Outline platelets.
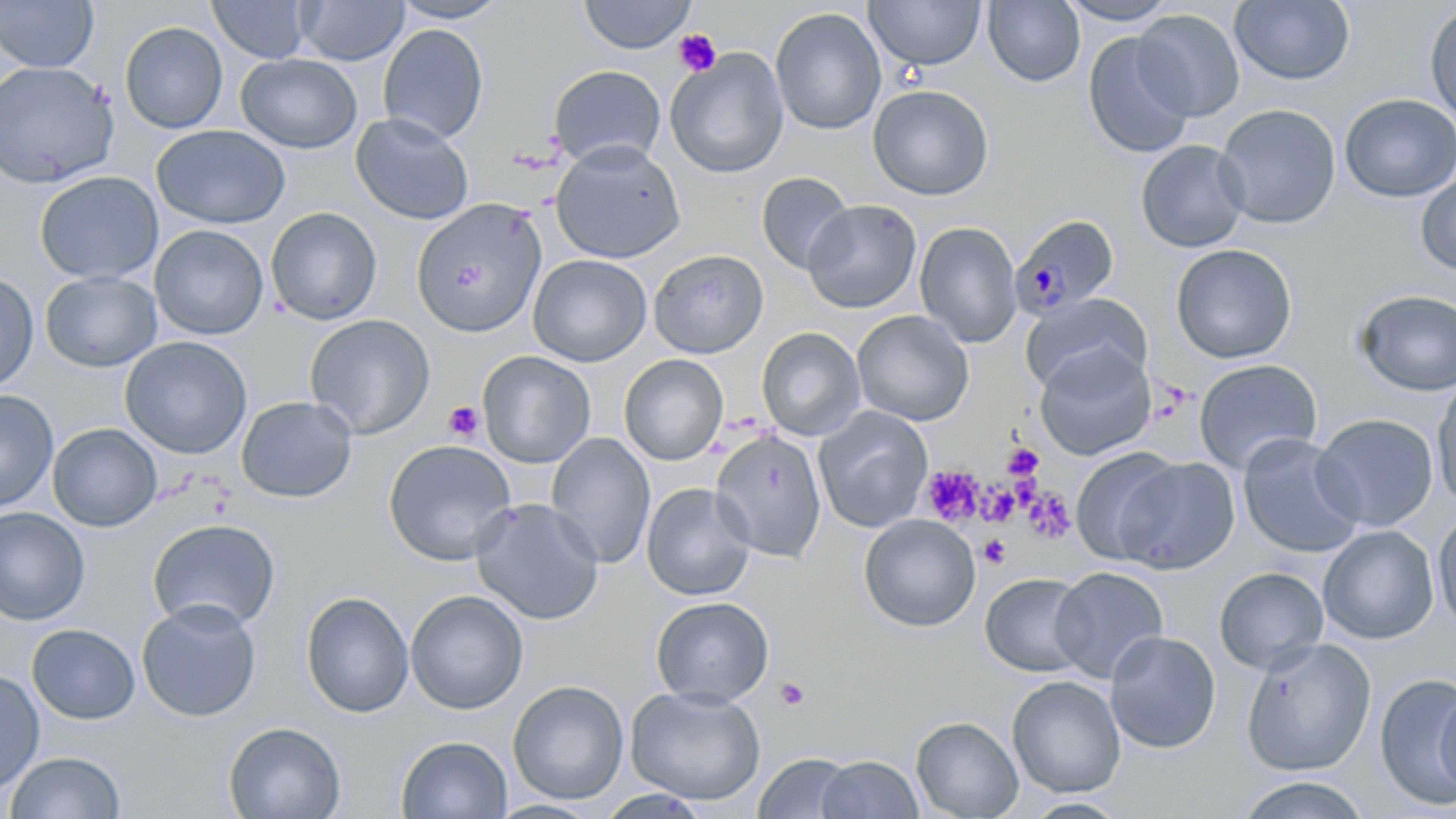
Approximate bounding boxes as (x1, y1, x2, y2) in pixels.
Platelets: (674, 29, 721, 76), (443, 401, 486, 443), (1002, 442, 1044, 480), (921, 466, 984, 524), (980, 483, 1020, 527), (1022, 488, 1075, 544), (978, 534, 1011, 568), (774, 678, 810, 711).

Plasmodium malariae-infected red blood cell locations = approximate bounding boxes as (x1, y1, x2, y2) in pixels: (1010, 213, 1120, 320)
slide-level diagnosis = Plasmodium malariae
uninfected red blood cell locations = approximate bounding boxes as (x1, y1, x2, y2) in pixels: (0, 0, 99, 72), (208, 0, 313, 63), (578, 0, 697, 54), (865, 0, 986, 71), (982, 0, 1085, 87), (1057, 0, 1180, 26), (1229, 0, 1354, 85), (295, 1, 409, 65), (389, 1, 510, 24), (1424, 3, 1456, 125), (770, 8, 886, 136), (1132, 9, 1244, 122), (120, 21, 228, 134), (378, 24, 489, 144), (1082, 32, 1195, 158), (666, 49, 789, 179), (236, 53, 363, 153), (0, 61, 119, 188), (548, 65, 666, 168), (867, 84, 994, 200), (1339, 94, 1456, 203), (1214, 104, 1341, 228), (350, 113, 475, 225), (151, 124, 290, 229), (1135, 139, 1251, 253), (550, 140, 686, 263), (35, 170, 163, 284), (756, 172, 855, 274), (1416, 172, 1456, 275), (411, 198, 548, 339), (803, 200, 922, 313), (265, 206, 382, 325), (915, 221, 1023, 348), (150, 224, 269, 340), (1170, 243, 1298, 363), (648, 249, 769, 358), (528, 254, 652, 366), (40, 271, 161, 372), (0, 272, 39, 393), (1354, 289, 1456, 397), (1021, 293, 1151, 394), (852, 310, 974, 426), (304, 314, 435, 439), (757, 327, 865, 441), (120, 336, 252, 459), (1035, 344, 1157, 460), (478, 351, 596, 468), (619, 355, 728, 465), (1194, 359, 1323, 475), (1431, 375, 1456, 508), (0, 389, 58, 512), (236, 396, 358, 503), (813, 406, 933, 533), (1311, 413, 1438, 532), (47, 423, 162, 532), (710, 430, 826, 562), (546, 433, 656, 569), (1237, 433, 1364, 559), (383, 439, 517, 566), (1071, 447, 1184, 565), (1115, 456, 1240, 574), (642, 482, 756, 601), (471, 498, 604, 626), (0, 507, 90, 626), (1433, 509, 1456, 632), (859, 514, 981, 632), (147, 518, 281, 632), (1318, 525, 1438, 644), (1049, 566, 1168, 684), (1214, 567, 1328, 673), (980, 573, 1092, 677), (406, 589, 528, 714), (300, 590, 415, 718), (650, 596, 774, 706), (137, 599, 261, 723), (27, 624, 140, 724), (1104, 630, 1221, 754), (1239, 637, 1377, 777), (0, 669, 45, 795), (1375, 672, 1456, 810), (1006, 675, 1126, 798), (507, 680, 629, 804), (1434, 680, 1456, 802), (625, 686, 767, 805), (911, 716, 1024, 819), (223, 721, 346, 819), (396, 735, 513, 818), (3, 751, 126, 818), (754, 753, 858, 818), (815, 755, 923, 818), (1235, 775, 1372, 818), (596, 790, 712, 818), (1019, 797, 1130, 818), (489, 799, 604, 818)
preparation = thin blood smear
stain = May-Grünwald-Giemsa
magnification = 1000x
image size = 1456×819 pixels
field of view = one of a larger specimen
modality = optical microscopy